Outline each Plasmodium falciparum parasite and classify it by life-cycle stage.
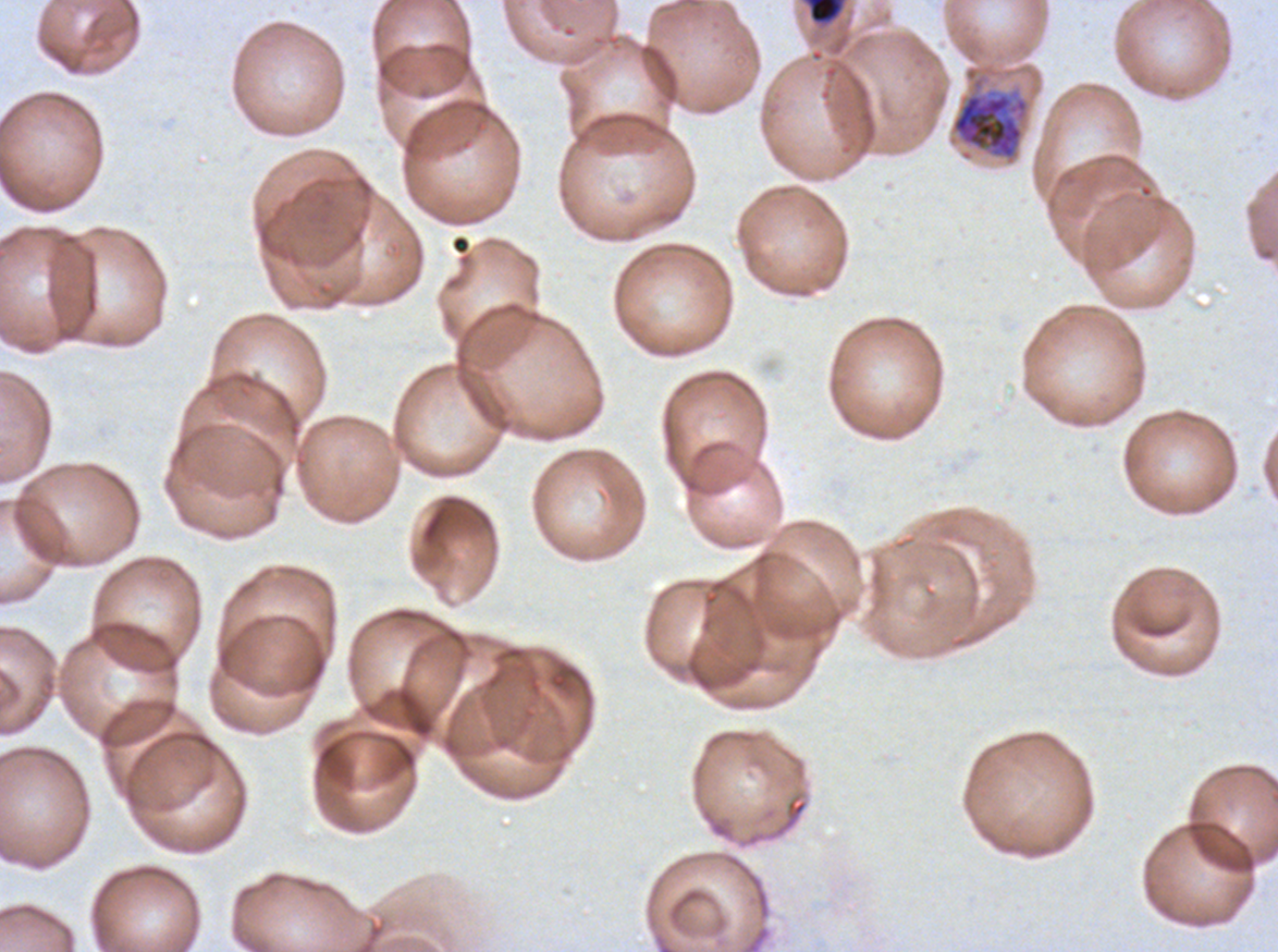
Approximate bounding boxes as [x1, y1, x2, y2] in pixels.
Mid trophozoites: [809, 0, 838, 22].
Early schizonts: [951, 92, 1029, 160].
No rings, late-ring/early-trophozoite forms, late trophozoites, late schizonts, segmenters, or gametocytes observed.

{
  "specimen": "ex-vivo Plasmodium falciparum culture from a patient in The Gambia, grown for 24 to 48 hours",
  "life_cycle_stages_observed": "mid trophozoite, early schizont",
  "preparation": "thin blood film",
  "image_size": "1278×952 pixels",
  "field_of_view": "one sub-image of a larger composite",
  "stain": "Giemsa"
}